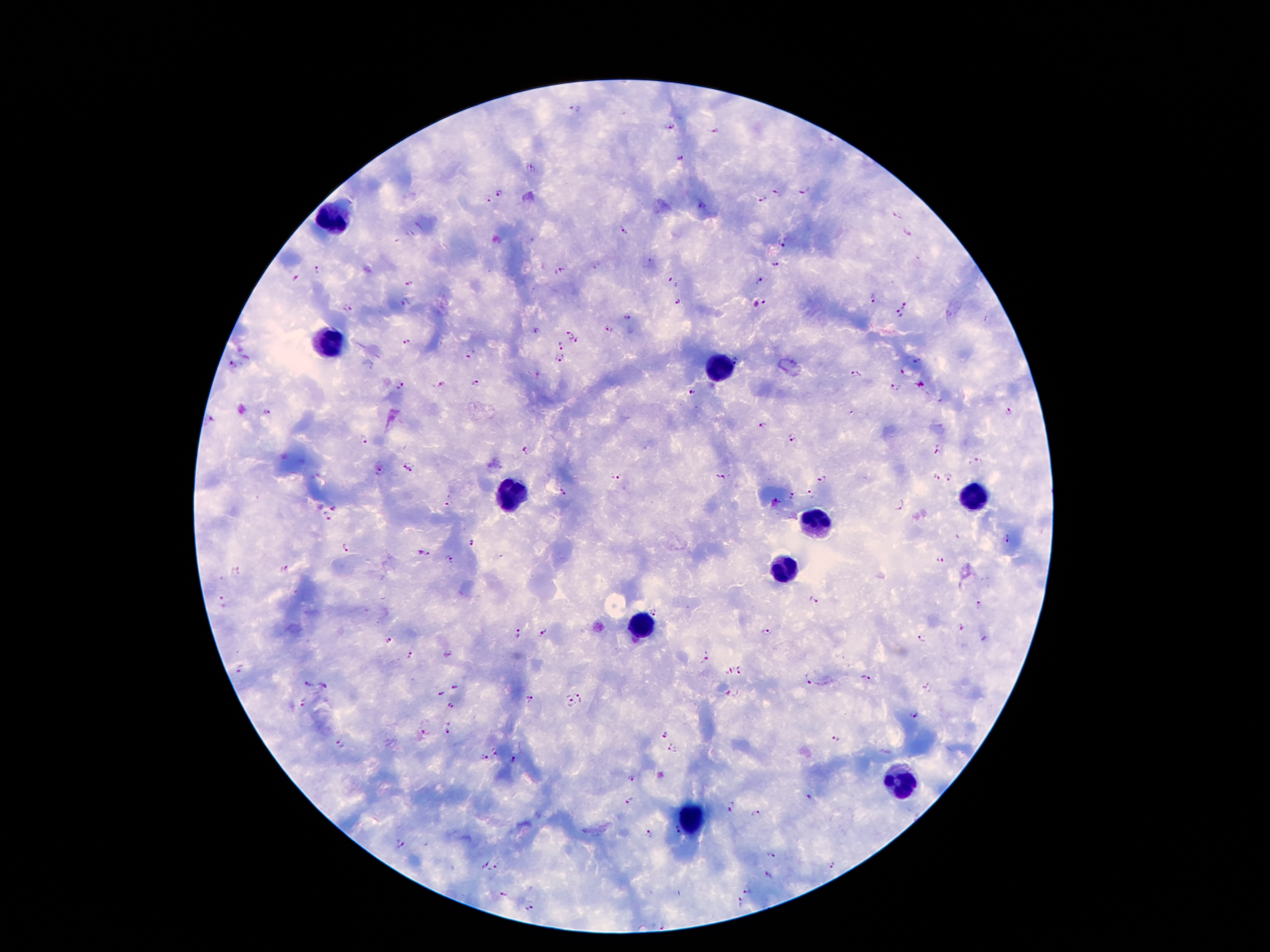
Approximate centers as [x, y] in pixels.
Summary:
  - Plasmodium parasite locations: [575, 110], [670, 127], [714, 131], [831, 139], [681, 159], [531, 169], [803, 191], [499, 192], [777, 192], [487, 198], [763, 198], [701, 206], [899, 215], [625, 231], [907, 234], [781, 242], [775, 264], [318, 269], [562, 270], [296, 279], [673, 279], [761, 280], [411, 283], [874, 299], [678, 301], [765, 301], [755, 303], [406, 304], [904, 306], [347, 308], [899, 314], [629, 317], [609, 329], [537, 331], [571, 331], [407, 341], [574, 342], [561, 344], [468, 356], [558, 358], [735, 360], [917, 360], [232, 366], [903, 371], [855, 373], [477, 383], [922, 384], [442, 385], [402, 386], [896, 387], [693, 392], [1009, 411], [267, 412], [211, 418], [762, 424], [792, 436], [364, 439], [525, 450], [939, 451], [978, 461], [403, 463], [412, 470], [381, 471], [949, 476], [615, 477], [721, 477], [936, 477], [822, 479], [812, 492], [563, 493], [792, 495], [779, 497], [900, 505], [447, 506], [334, 508], [326, 518], [1007, 540], [472, 543], [344, 547], [419, 553], [429, 553], [450, 560], [940, 560], [284, 568], [237, 572], [814, 598], [224, 602], [978, 605], [655, 609], [962, 627], [545, 632], [766, 632], [517, 634], [922, 637], [388, 640], [409, 655], [706, 658], [742, 669], [241, 670], [729, 671], [865, 677], [808, 678], [309, 684], [324, 686], [454, 688], [927, 689], [440, 694], [580, 695], [531, 698], [302, 704], [572, 704], [451, 706], [913, 714], [448, 729], [426, 731], [664, 734], [836, 739], [341, 744], [673, 748], [496, 750], [483, 758], [513, 760], [631, 778], [808, 797], [733, 800], [631, 801], [729, 810], [757, 813], [677, 831], [649, 834], [399, 844], [769, 854], [497, 865], [832, 866], [487, 867], [769, 876], [748, 889], [504, 893], [741, 903], [530, 908], [664, 926]
  - Leukocyte locations: [339, 218], [330, 344], [715, 369], [515, 492], [967, 497], [816, 522], [784, 571], [643, 628], [896, 781], [690, 819]
  - Patient malaria status: infected with Plasmodium falciparum
  - Magnification: 100x
  - Image size: 1270×952 pixels
  - Capture: smartphone camera through the microscope eyepiece
  - Preparation: thick peripheral-blood smear
  - Stain: Giemsa
  - Field of view: single